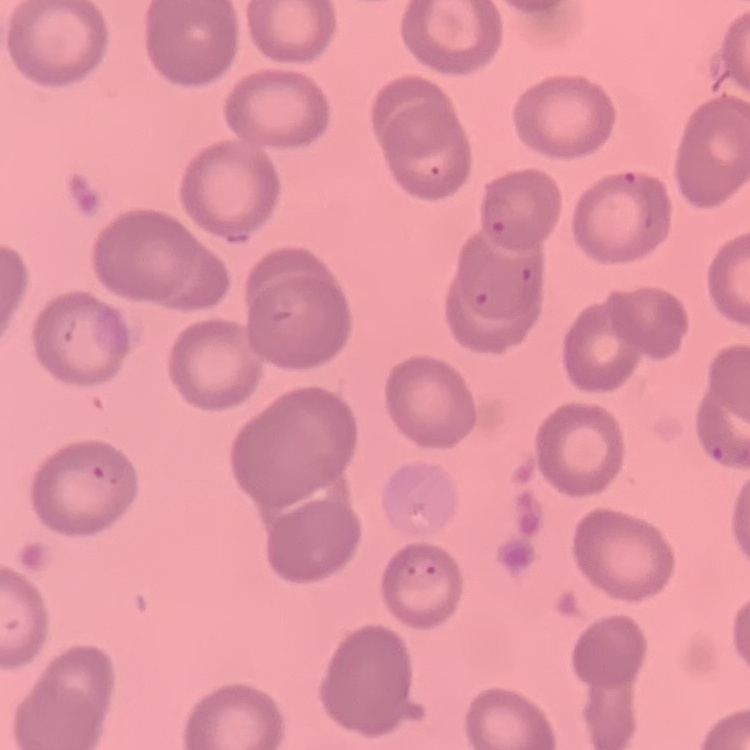
red blood cell morphology = no rouleaux formation
image type = square crop of a larger photomicrograph
preparation = thin blood smear
stain = Field's or Giemsa